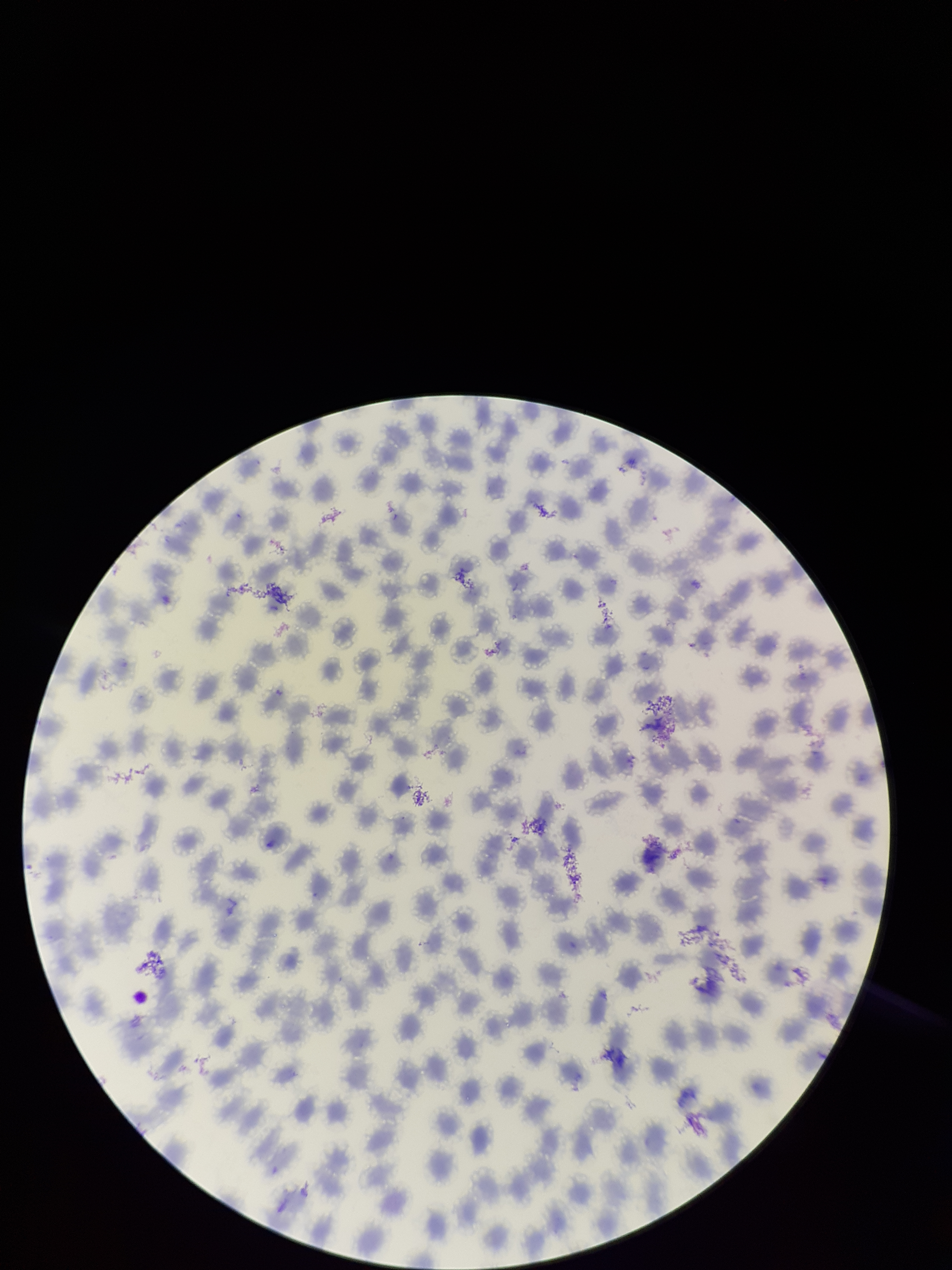
Parasitized red blood cells: none detected. Photographed through the microscope eyepiece with a smartphone camera. Giemsa stain. Preparation: thin blood smear. Patient malaria status: infected. Single field of view. Red blood cell count: 233. Species reported for this patient: Plasmodium vivax. Parasitized red blood cell count: 0. Image is 952×1270 pixels.